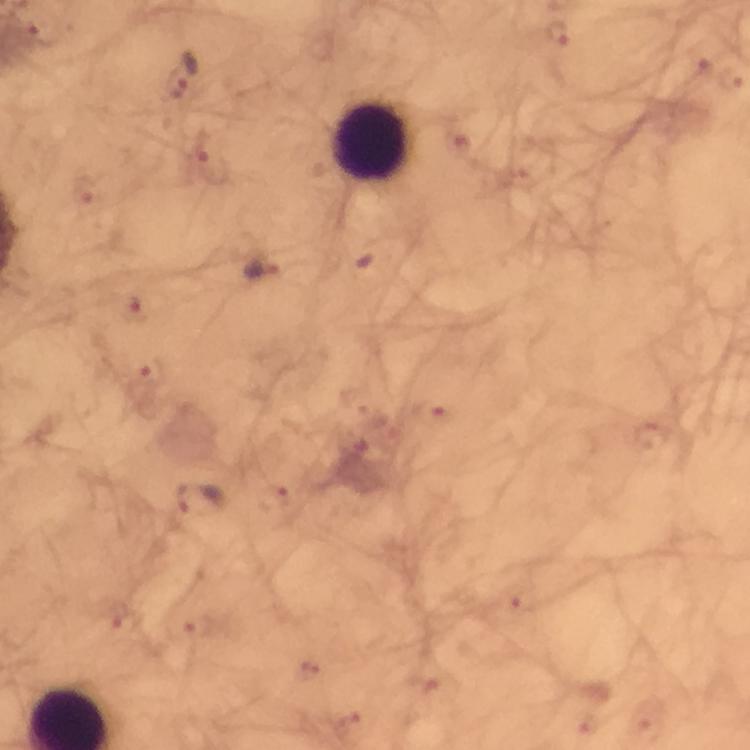
Approximate object centers, in pixels from the top-left corner. Leukocyte locations: (x=371, y=142). Malaria parasite locations: (x=558, y=36), (x=699, y=63), (x=729, y=80), (x=176, y=84), (x=210, y=160), (x=84, y=190), (x=259, y=270), (x=136, y=309), (x=149, y=371), (x=434, y=414), (x=652, y=436), (x=273, y=498), (x=201, y=500), (x=507, y=601), (x=127, y=625), (x=197, y=629), (x=309, y=671), (x=424, y=684), (x=350, y=725), (x=650, y=725), (x=583, y=726). Image is 750×750 pixels. Giemsa-stained preparation. A crop from one field of view. Immersion oil was used. From a diagnostic examination for malaria. Thick smear. Smartphone photograph taken through a microscope. 100x magnification.